Classify this cell by malaria status.
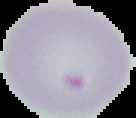
It is parasitized.

Summary:
  - Preparation: thin blood smear
  - Image type: segmented cell region with the area outside set to black
  - Image size: 136×118 pixels